Identify the blood parasite species.
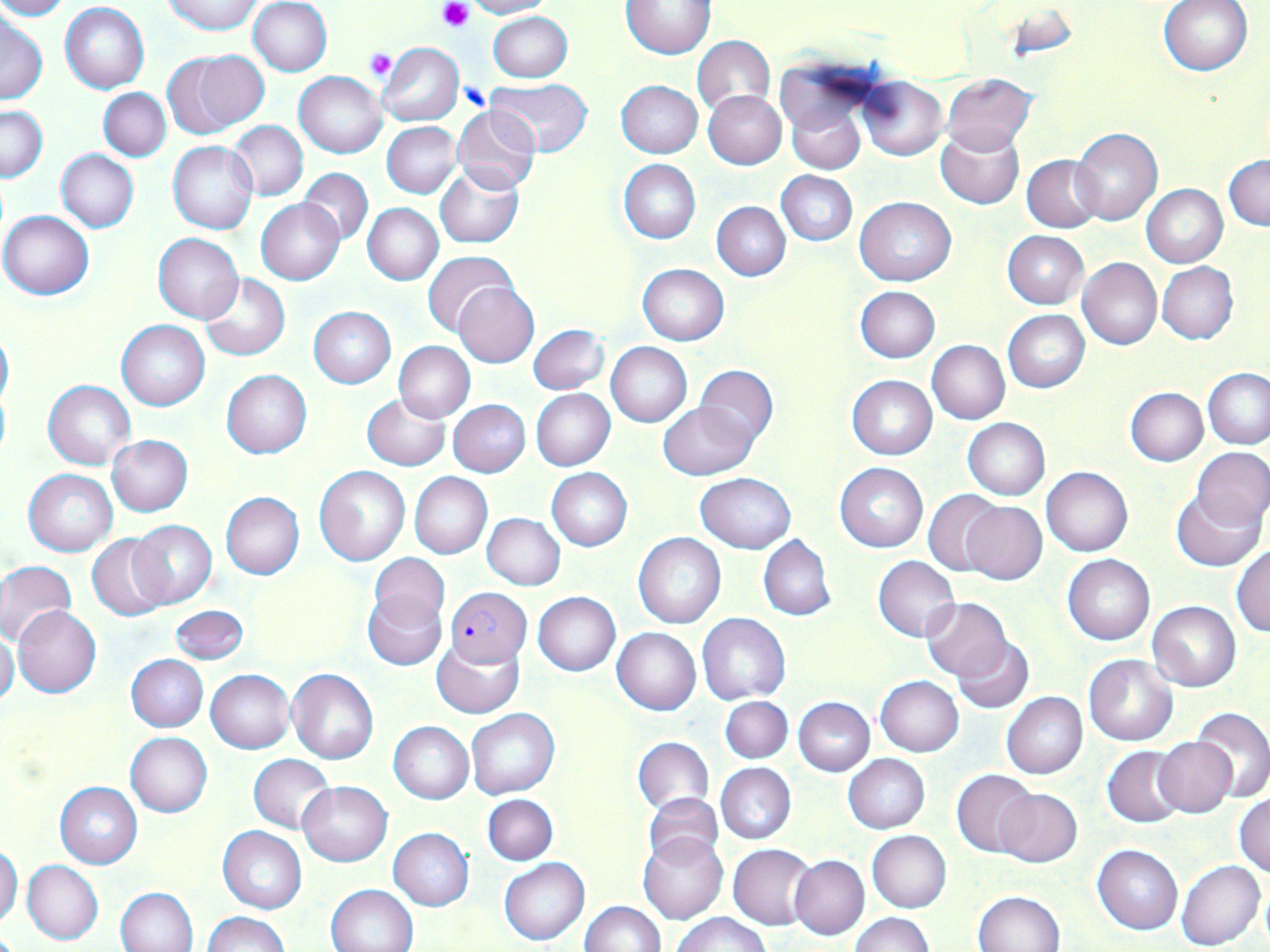

Plasmodium falciparum.

Summary:
  - Coordinate format: approximate bounding boxes as named x1/y1/x2/y2 corners in pixels
  - Plasmodium falciparum-infected red blood cell locations: (x1=444, y1=586, x2=531, y2=666)
  - Uninfected red blood cell locations: (x1=0, y1=0, x2=71, y2=20), (x1=163, y1=0, x2=263, y2=34), (x1=249, y1=0, x2=332, y2=76), (x1=465, y1=0, x2=553, y2=19), (x1=1158, y1=0, x2=1252, y2=76), (x1=621, y1=1, x2=714, y2=59), (x1=61, y1=3, x2=149, y2=93), (x1=486, y1=11, x2=572, y2=82), (x1=0, y1=12, x2=47, y2=105), (x1=692, y1=36, x2=774, y2=117), (x1=377, y1=40, x2=463, y2=126), (x1=164, y1=48, x2=268, y2=138), (x1=294, y1=71, x2=388, y2=159), (x1=944, y1=74, x2=1036, y2=154), (x1=856, y1=76, x2=947, y2=161), (x1=485, y1=79, x2=593, y2=157), (x1=615, y1=80, x2=703, y2=158), (x1=98, y1=87, x2=171, y2=160), (x1=703, y1=90, x2=786, y2=170), (x1=786, y1=98, x2=866, y2=175), (x1=0, y1=104, x2=47, y2=182), (x1=452, y1=106, x2=541, y2=195), (x1=228, y1=121, x2=308, y2=201), (x1=382, y1=121, x2=462, y2=198), (x1=935, y1=126, x2=1024, y2=209), (x1=1071, y1=127, x2=1162, y2=226), (x1=167, y1=141, x2=257, y2=234), (x1=56, y1=149, x2=138, y2=233), (x1=1021, y1=154, x2=1104, y2=232), (x1=1224, y1=154, x2=1270, y2=230), (x1=619, y1=158, x2=701, y2=243), (x1=435, y1=164, x2=524, y2=249), (x1=299, y1=168, x2=373, y2=246), (x1=776, y1=171, x2=857, y2=246), (x1=1141, y1=184, x2=1227, y2=268), (x1=855, y1=197, x2=956, y2=286), (x1=256, y1=199, x2=345, y2=284), (x1=712, y1=202, x2=790, y2=281), (x1=362, y1=203, x2=444, y2=285), (x1=1, y1=210, x2=94, y2=299), (x1=1003, y1=230, x2=1088, y2=309), (x1=153, y1=233, x2=242, y2=322), (x1=422, y1=250, x2=519, y2=337), (x1=1077, y1=259, x2=1161, y2=350), (x1=1157, y1=261, x2=1238, y2=344), (x1=637, y1=263, x2=729, y2=345), (x1=198, y1=273, x2=290, y2=361), (x1=454, y1=281, x2=538, y2=367), (x1=856, y1=285, x2=941, y2=362), (x1=308, y1=306, x2=396, y2=387), (x1=1003, y1=309, x2=1090, y2=393), (x1=117, y1=320, x2=210, y2=410), (x1=530, y1=324, x2=608, y2=394), (x1=0, y1=326, x2=13, y2=411), (x1=393, y1=340, x2=475, y2=422), (x1=927, y1=340, x2=1010, y2=422), (x1=606, y1=342, x2=691, y2=427), (x1=693, y1=366, x2=778, y2=449), (x1=1203, y1=368, x2=1270, y2=449), (x1=222, y1=369, x2=311, y2=459), (x1=847, y1=374, x2=937, y2=460), (x1=44, y1=380, x2=136, y2=470), (x1=1125, y1=387, x2=1208, y2=466), (x1=531, y1=388, x2=615, y2=470), (x1=361, y1=394, x2=450, y2=471), (x1=449, y1=400, x2=530, y2=477), (x1=658, y1=401, x2=755, y2=480), (x1=963, y1=418, x2=1049, y2=499), (x1=107, y1=435, x2=193, y2=515), (x1=1193, y1=447, x2=1270, y2=528), (x1=834, y1=462, x2=928, y2=552), (x1=314, y1=466, x2=409, y2=566), (x1=1041, y1=466, x2=1132, y2=557), (x1=547, y1=467, x2=632, y2=550), (x1=24, y1=469, x2=117, y2=556), (x1=1053, y1=469, x2=1141, y2=646), (x1=409, y1=472, x2=492, y2=558), (x1=696, y1=473, x2=796, y2=553), (x1=924, y1=489, x2=1007, y2=575), (x1=1171, y1=491, x2=1264, y2=571), (x1=220, y1=492, x2=304, y2=579), (x1=960, y1=501, x2=1046, y2=586), (x1=482, y1=513, x2=565, y2=590), (x1=125, y1=519, x2=216, y2=609), (x1=87, y1=533, x2=171, y2=620), (x1=633, y1=533, x2=726, y2=629), (x1=758, y1=535, x2=836, y2=620), (x1=1231, y1=546, x2=1270, y2=636), (x1=369, y1=553, x2=450, y2=629), (x1=1063, y1=554, x2=1154, y2=644), (x1=872, y1=556, x2=959, y2=642), (x1=0, y1=561, x2=76, y2=647), (x1=363, y1=590, x2=446, y2=670), (x1=532, y1=591, x2=620, y2=675), (x1=921, y1=597, x2=1012, y2=680), (x1=1147, y1=601, x2=1241, y2=692), (x1=171, y1=605, x2=249, y2=663), (x1=14, y1=606, x2=102, y2=698), (x1=698, y1=613, x2=790, y2=703), (x1=612, y1=627, x2=701, y2=715), (x1=0, y1=629, x2=20, y2=707), (x1=951, y1=636, x2=1034, y2=714), (x1=432, y1=637, x2=523, y2=719), (x1=127, y1=655, x2=207, y2=731), (x1=1084, y1=655, x2=1177, y2=745), (x1=288, y1=668, x2=379, y2=764), (x1=206, y1=669, x2=294, y2=753), (x1=876, y1=676, x2=963, y2=756), (x1=1001, y1=691, x2=1087, y2=779), (x1=720, y1=695, x2=793, y2=762), (x1=794, y1=696, x2=875, y2=775), (x1=1192, y1=707, x2=1270, y2=803), (x1=467, y1=709, x2=558, y2=798), (x1=389, y1=721, x2=474, y2=802), (x1=125, y1=732, x2=213, y2=816), (x1=632, y1=736, x2=714, y2=814), (x1=1153, y1=737, x2=1238, y2=818), (x1=1102, y1=746, x2=1188, y2=828), (x1=248, y1=754, x2=336, y2=833), (x1=843, y1=754, x2=930, y2=833), (x1=716, y1=763, x2=796, y2=844), (x1=952, y1=768, x2=1038, y2=857), (x1=297, y1=780, x2=392, y2=866), (x1=56, y1=782, x2=142, y2=868), (x1=993, y1=787, x2=1082, y2=867), (x1=1234, y1=791, x2=1270, y2=877), (x1=642, y1=792, x2=723, y2=868), (x1=483, y1=794, x2=557, y2=865), (x1=218, y1=826, x2=306, y2=914), (x1=388, y1=828, x2=474, y2=911), (x1=638, y1=831, x2=728, y2=923), (x1=867, y1=831, x2=951, y2=912), (x1=0, y1=845, x2=23, y2=928), (x1=727, y1=845, x2=815, y2=929), (x1=1092, y1=845, x2=1183, y2=934), (x1=790, y1=855, x2=869, y2=939), (x1=499, y1=857, x2=589, y2=945), (x1=22, y1=860, x2=103, y2=945), (x1=1176, y1=860, x2=1266, y2=950), (x1=326, y1=884, x2=417, y2=952), (x1=116, y1=887, x2=198, y2=951), (x1=973, y1=890, x2=1066, y2=952), (x1=579, y1=901, x2=666, y2=952), (x1=201, y1=912, x2=292, y2=952), (x1=674, y1=912, x2=771, y2=952), (x1=851, y1=913, x2=932, y2=951)
  - Platelet locations: (x1=437, y1=0, x2=474, y2=33), (x1=364, y1=48, x2=399, y2=83), (x1=460, y1=81, x2=493, y2=112)
  - Image size: 1270×952 pixels
  - Stain: May-Grünwald-Giemsa
  - Preparation: thin blood film
  - Modality: light microscopy
  - Magnification: 1000x
  - Field of view: one of a larger specimen